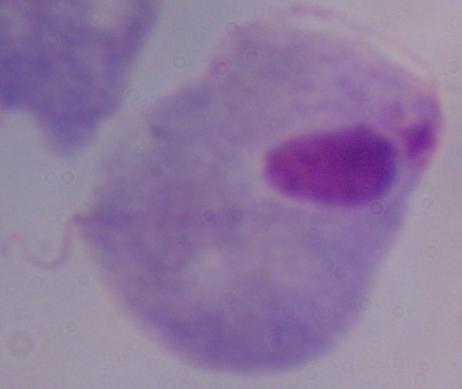 Photomicrograph. A trichomonad is seen. 1000x magnification.